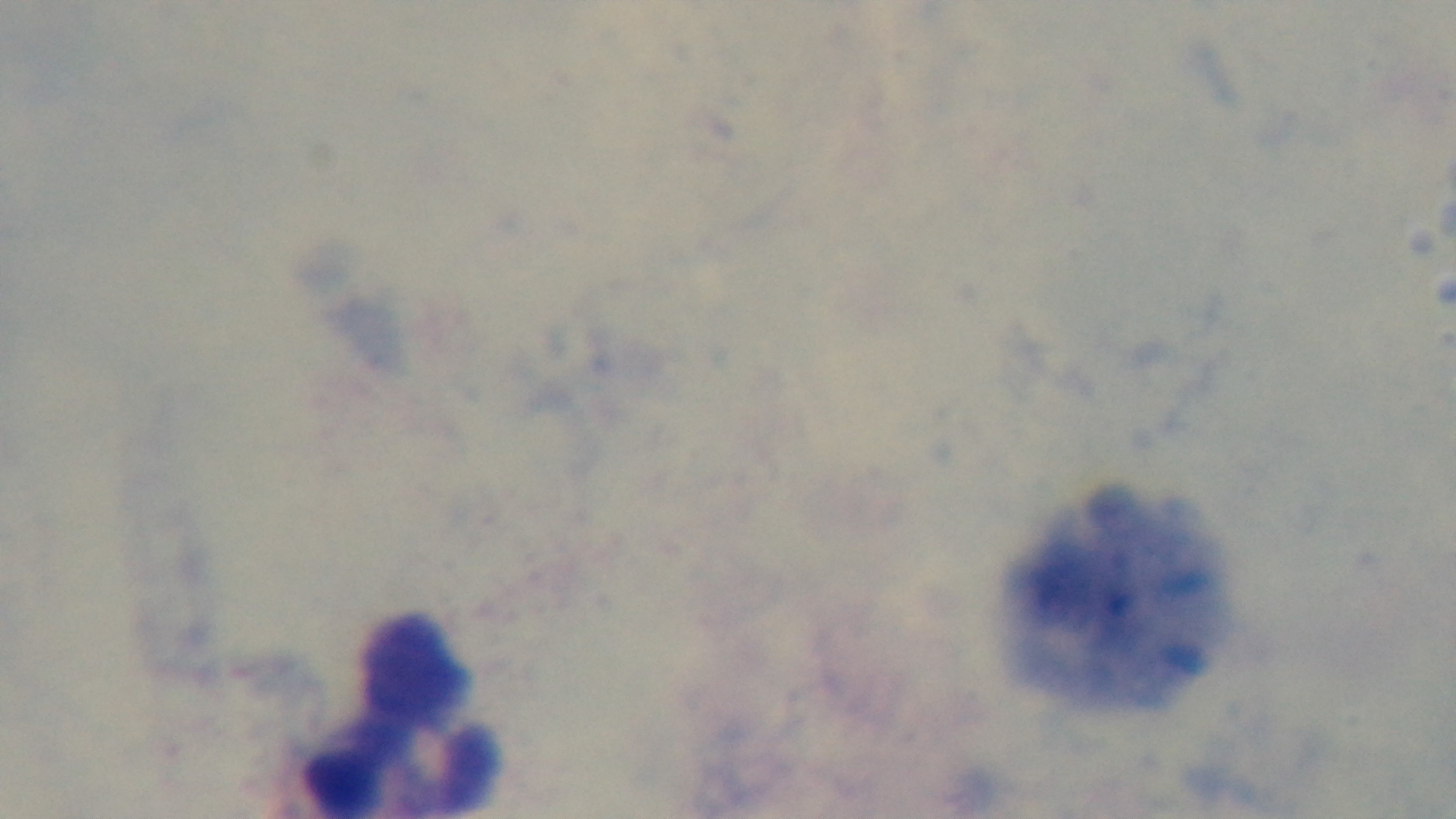 Single field of view. Oil-immersion objective, 100x. Giemsa-stained. Captured with a mounted 4K digital camera. Light microscopy. Malaria status: negative. Preparation: thick.